Give the extent of all uninfected red blood cells.
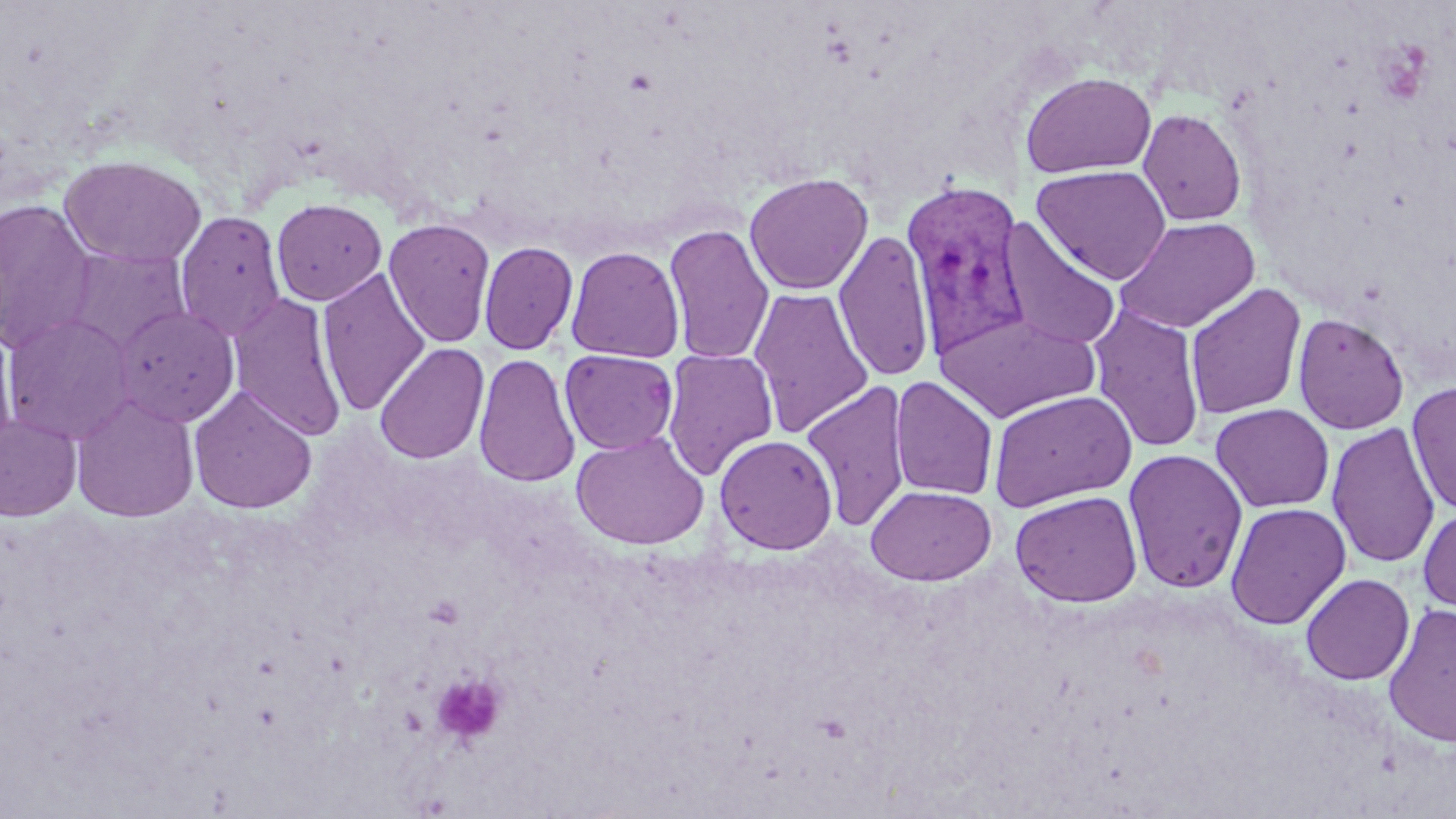
Approximate bounding boxes as named x1/y1/x2/y2 corners in pixels.
Uninfected red blood cells: (x1=1020, y1=71, x2=1157, y2=178), (x1=1137, y1=108, x2=1247, y2=226), (x1=59, y1=154, x2=207, y2=268), (x1=1031, y1=164, x2=1172, y2=284), (x1=744, y1=171, x2=873, y2=295), (x1=0, y1=198, x2=99, y2=353), (x1=271, y1=198, x2=387, y2=305), (x1=175, y1=211, x2=287, y2=342), (x1=1115, y1=217, x2=1260, y2=334), (x1=384, y1=218, x2=497, y2=348), (x1=998, y1=219, x2=1121, y2=351), (x1=663, y1=223, x2=775, y2=364), (x1=834, y1=229, x2=936, y2=382), (x1=479, y1=241, x2=578, y2=355), (x1=565, y1=245, x2=686, y2=363), (x1=61, y1=246, x2=191, y2=356), (x1=317, y1=268, x2=431, y2=416), (x1=1184, y1=284, x2=1306, y2=420), (x1=749, y1=287, x2=875, y2=438), (x1=228, y1=293, x2=348, y2=442), (x1=1088, y1=303, x2=1207, y2=453), (x1=112, y1=305, x2=242, y2=428), (x1=934, y1=311, x2=1100, y2=422), (x1=1, y1=312, x2=136, y2=444), (x1=1293, y1=313, x2=1409, y2=434), (x1=0, y1=328, x2=18, y2=461), (x1=374, y1=342, x2=490, y2=465), (x1=559, y1=349, x2=678, y2=455), (x1=661, y1=349, x2=778, y2=480), (x1=473, y1=352, x2=580, y2=488), (x1=889, y1=376, x2=998, y2=500), (x1=802, y1=380, x2=911, y2=531), (x1=1406, y1=382, x2=1456, y2=516), (x1=188, y1=386, x2=318, y2=514), (x1=989, y1=389, x2=1137, y2=510), (x1=70, y1=393, x2=199, y2=522), (x1=1211, y1=403, x2=1334, y2=513), (x1=0, y1=413, x2=83, y2=522), (x1=1327, y1=420, x2=1441, y2=569), (x1=570, y1=430, x2=710, y2=550), (x1=714, y1=433, x2=838, y2=554), (x1=1123, y1=448, x2=1248, y2=594), (x1=866, y1=484, x2=996, y2=585), (x1=1010, y1=490, x2=1143, y2=608), (x1=1225, y1=501, x2=1350, y2=630), (x1=1417, y1=505, x2=1456, y2=617), (x1=1301, y1=573, x2=1415, y2=685), (x1=1382, y1=602, x2=1456, y2=748).

slide-level diagnosis = Plasmodium vivax
field of view = single
stain = May-Grünwald-Giemsa
platelet locations = approximate bounding boxes as named x1/y1/x2/y2 corners in pixels: (x1=430, y1=672, x2=508, y2=747)
modality = light microscopy
magnification = 1000x
preparation = thin blood film
Plasmodium vivax-infected red blood cell locations = approximate bounding boxes as named x1/y1/x2/y2 corners in pixels: (x1=900, y1=180, x2=1032, y2=360)
image size = 1456×819 pixels